Report the malaria status of this cell.
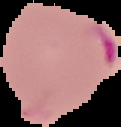

Parasitized.

Summary:
  - Image type: segmented cell region with the area outside set to black
  - Preparation: thin blood smear
  - Image size: 121×127 pixels